Classify this cell by malaria status.
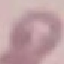

Uninfected.

Summary:
  - Capture: smartphone camera at the microscope eyepiece
  - Preparation: thin blood smear
  - Stain: Giemsa
  - Image type: automatically extracted cell patch, resized to 64 × 64 pixels